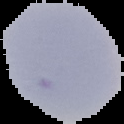
From a thin blood film. Malaria status: uninfected. Image is 124×124 pixels. The area outside the segmented cell region is set to black.